Assess this cell for malaria.
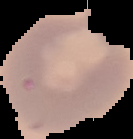

It is uninfected.

Summary:
  - Preparation: thin blood smear
  - Image size: 133×139 pixels
  - Image type: segmented cell region with the area outside set to black